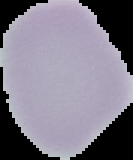
Summary:
  - Image size: 133×160 pixels
  - Image type: cell region segmented out of the field of view; surrounding area masked to black
  - Preparation: thin blood smear
  - Result: no malaria parasites detected